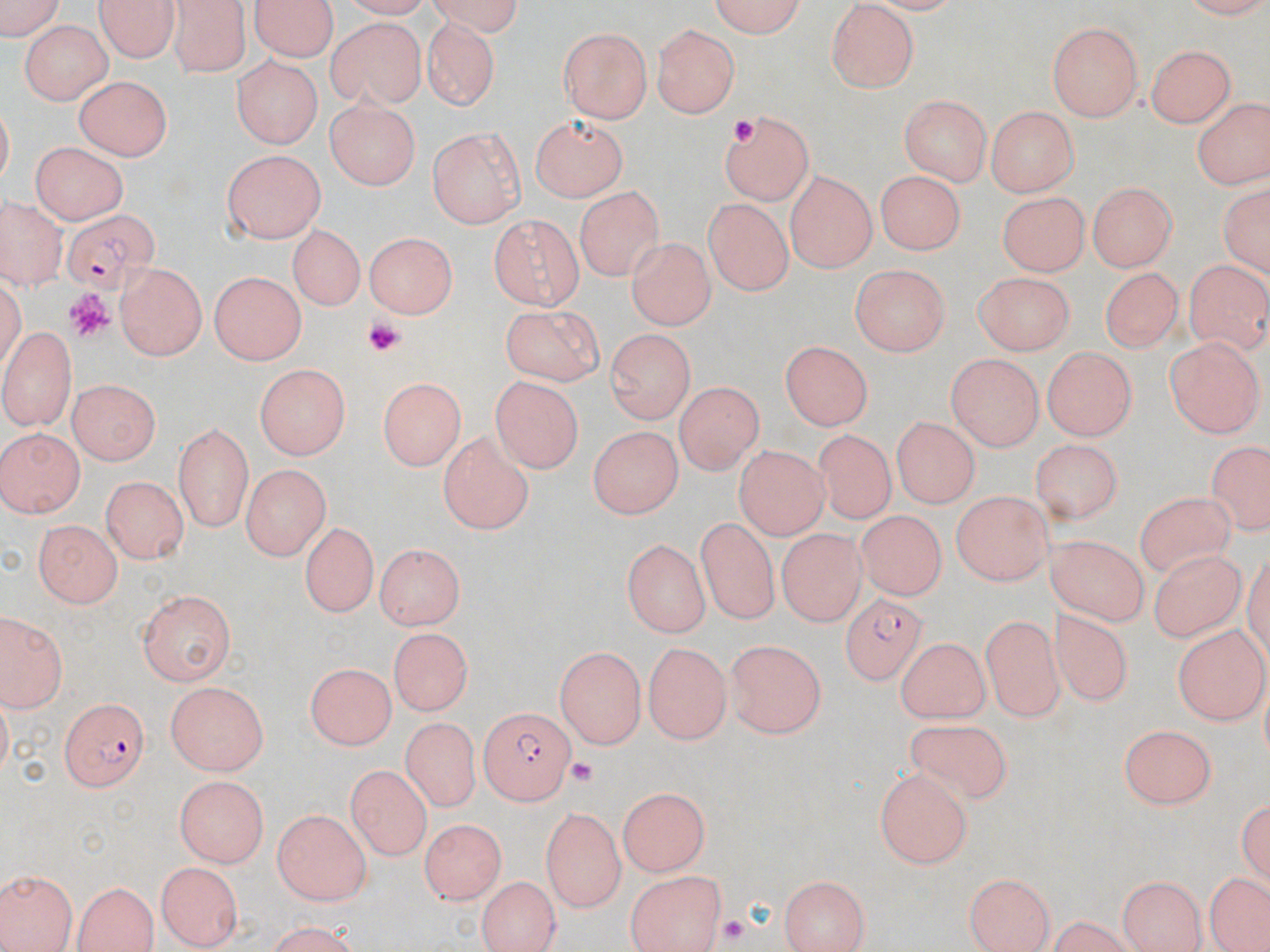
Approximate bounding boxes as named x1/y1/x2/y2 corners in pixels. Plasmodium falciparum-infected red blood cell locations: (x1=61, y1=207, x2=160, y2=293), (x1=842, y1=599, x2=930, y2=690), (x1=56, y1=698, x2=152, y2=790), (x1=479, y1=706, x2=578, y2=803). Platelet locations: (x1=728, y1=115, x2=762, y2=150), (x1=63, y1=290, x2=116, y2=340), (x1=364, y1=318, x2=403, y2=356), (x1=559, y1=758, x2=602, y2=787), (x1=719, y1=915, x2=748, y2=942). Uninfected red blood cell locations: (x1=97, y1=0, x2=177, y2=65), (x1=251, y1=0, x2=335, y2=63), (x1=706, y1=0, x2=813, y2=39), (x1=2, y1=2, x2=61, y2=46), (x1=169, y1=3, x2=249, y2=79), (x1=821, y1=3, x2=916, y2=95), (x1=29, y1=9, x2=183, y2=77), (x1=421, y1=11, x2=509, y2=113), (x1=20, y1=19, x2=110, y2=107), (x1=329, y1=20, x2=427, y2=113), (x1=652, y1=23, x2=740, y2=119), (x1=1047, y1=23, x2=1144, y2=120), (x1=557, y1=26, x2=654, y2=122), (x1=1147, y1=43, x2=1235, y2=128), (x1=232, y1=58, x2=320, y2=148), (x1=73, y1=72, x2=174, y2=162), (x1=900, y1=95, x2=990, y2=188), (x1=1190, y1=95, x2=1268, y2=191), (x1=323, y1=99, x2=422, y2=188), (x1=989, y1=105, x2=1080, y2=194), (x1=719, y1=110, x2=816, y2=206), (x1=529, y1=114, x2=627, y2=201), (x1=426, y1=127, x2=525, y2=229), (x1=24, y1=142, x2=130, y2=224), (x1=222, y1=148, x2=328, y2=246), (x1=877, y1=167, x2=970, y2=254), (x1=785, y1=172, x2=874, y2=273), (x1=1089, y1=180, x2=1178, y2=272), (x1=577, y1=183, x2=661, y2=282), (x1=1217, y1=183, x2=1268, y2=282), (x1=995, y1=189, x2=1087, y2=275), (x1=703, y1=196, x2=796, y2=297), (x1=1, y1=197, x2=70, y2=286), (x1=490, y1=215, x2=584, y2=309), (x1=288, y1=223, x2=363, y2=313), (x1=367, y1=230, x2=459, y2=316), (x1=625, y1=234, x2=713, y2=328), (x1=1184, y1=259, x2=1269, y2=355), (x1=113, y1=263, x2=209, y2=361), (x1=849, y1=263, x2=949, y2=358), (x1=1098, y1=263, x2=1184, y2=350), (x1=208, y1=271, x2=306, y2=366), (x1=974, y1=271, x2=1072, y2=356), (x1=498, y1=307, x2=605, y2=385), (x1=0, y1=327, x2=78, y2=430), (x1=606, y1=330, x2=692, y2=425), (x1=1166, y1=336, x2=1262, y2=436), (x1=777, y1=339, x2=870, y2=429), (x1=1042, y1=346, x2=1134, y2=442), (x1=944, y1=353, x2=1041, y2=451), (x1=255, y1=364, x2=351, y2=458), (x1=488, y1=373, x2=580, y2=472), (x1=379, y1=378, x2=462, y2=473), (x1=69, y1=380, x2=161, y2=464), (x1=674, y1=383, x2=765, y2=473), (x1=890, y1=418, x2=979, y2=509), (x1=590, y1=421, x2=687, y2=518), (x1=173, y1=422, x2=253, y2=531), (x1=0, y1=427, x2=83, y2=519), (x1=810, y1=428, x2=901, y2=524), (x1=438, y1=432, x2=535, y2=535), (x1=1029, y1=436, x2=1122, y2=527), (x1=1205, y1=440, x2=1269, y2=537), (x1=734, y1=445, x2=830, y2=538), (x1=240, y1=465, x2=325, y2=558), (x1=103, y1=474, x2=187, y2=565), (x1=1134, y1=490, x2=1239, y2=578), (x1=949, y1=492, x2=1055, y2=585), (x1=857, y1=510, x2=944, y2=602), (x1=32, y1=518, x2=124, y2=609), (x1=300, y1=518, x2=378, y2=613), (x1=691, y1=518, x2=782, y2=632), (x1=775, y1=522, x2=868, y2=625), (x1=1047, y1=531, x2=1149, y2=628), (x1=622, y1=537, x2=707, y2=636), (x1=371, y1=545, x2=467, y2=627), (x1=1141, y1=551, x2=1255, y2=648), (x1=136, y1=589, x2=234, y2=685), (x1=1046, y1=607, x2=1135, y2=714), (x1=0, y1=608, x2=70, y2=715), (x1=979, y1=612, x2=1066, y2=722), (x1=1175, y1=625, x2=1268, y2=722), (x1=390, y1=626, x2=473, y2=716), (x1=893, y1=636, x2=988, y2=725), (x1=726, y1=637, x2=826, y2=737), (x1=645, y1=640, x2=730, y2=740), (x1=554, y1=644, x2=645, y2=746), (x1=305, y1=661, x2=394, y2=747), (x1=164, y1=681, x2=272, y2=775), (x1=400, y1=715, x2=480, y2=812), (x1=896, y1=719, x2=1018, y2=803), (x1=1117, y1=725, x2=1218, y2=810), (x1=344, y1=765, x2=429, y2=858), (x1=874, y1=767, x2=974, y2=869), (x1=174, y1=774, x2=272, y2=865), (x1=619, y1=786, x2=712, y2=872), (x1=1237, y1=792, x2=1270, y2=884), (x1=540, y1=806, x2=626, y2=911), (x1=273, y1=809, x2=373, y2=903), (x1=420, y1=816, x2=505, y2=905), (x1=155, y1=860, x2=239, y2=948), (x1=1, y1=866, x2=75, y2=952), (x1=625, y1=869, x2=727, y2=952), (x1=963, y1=870, x2=1057, y2=952), (x1=475, y1=874, x2=559, y2=952), (x1=780, y1=874, x2=870, y2=952), (x1=1118, y1=874, x2=1204, y2=952), (x1=1208, y1=874, x2=1266, y2=949), (x1=71, y1=878, x2=157, y2=952), (x1=1037, y1=916, x2=1142, y2=951). Slide-level diagnosis: Plasmodium falciparum. Image is 1270×952 pixels. May-Grünwald-Giemsa stain. Thin blood smear. Captured at 1000x magnification. Optical microscopy. Single field of view.